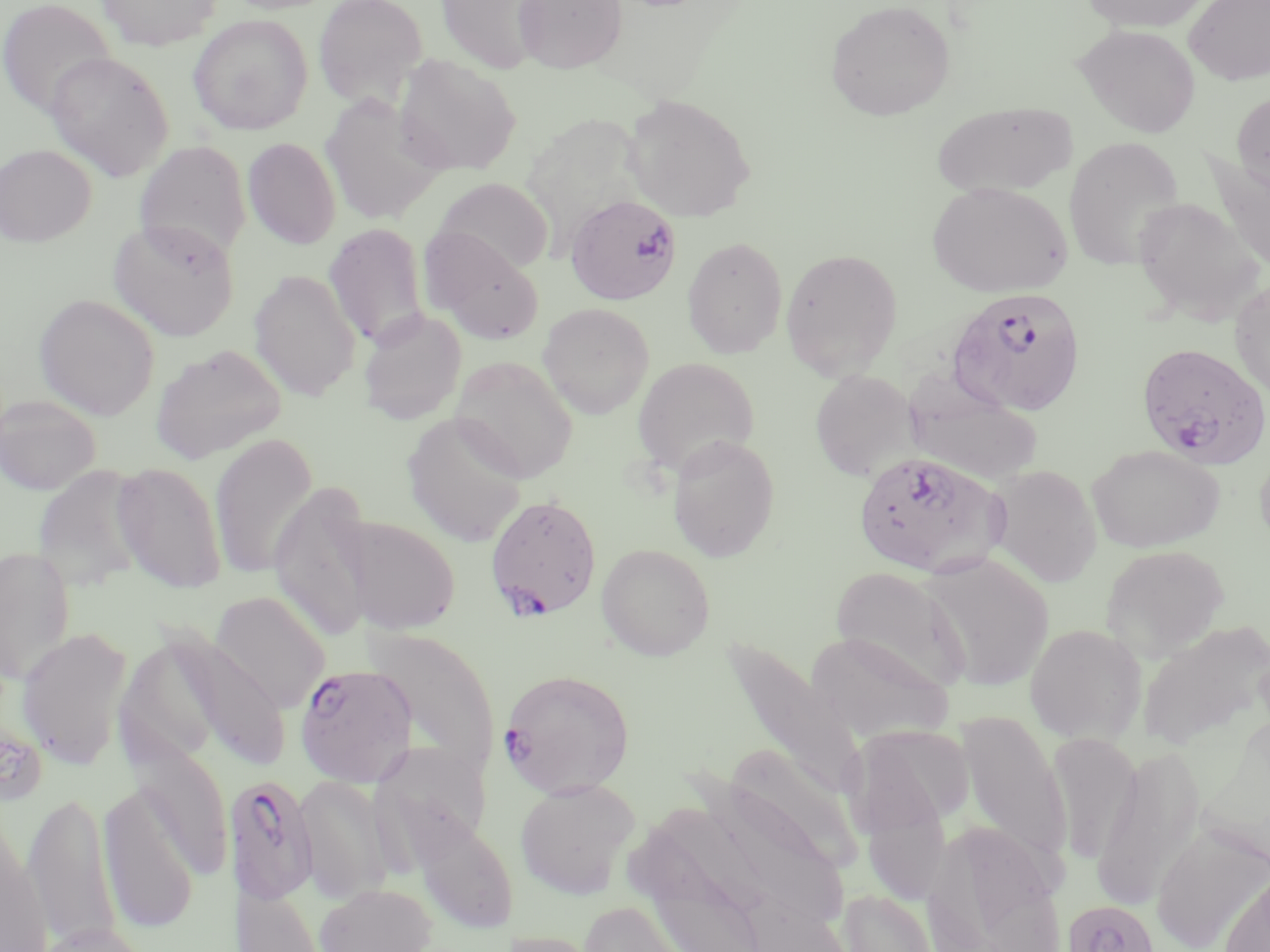

Approximate bounding boxes as [x1, y1, x2, y2] in pixels. Uninfected red blood cell locations: [96, 0, 221, 51], [313, 0, 428, 110], [435, 0, 549, 74], [513, 0, 627, 74], [825, 0, 956, 121], [1080, 0, 1211, 32], [1185, 0, 1270, 85], [0, 1, 115, 118], [188, 14, 312, 135], [1075, 24, 1200, 138], [45, 51, 174, 182], [392, 53, 521, 177], [1232, 91, 1270, 195], [621, 93, 755, 222], [319, 94, 444, 223], [931, 101, 1076, 198], [521, 114, 656, 235], [1063, 135, 1185, 271], [243, 137, 341, 249], [134, 140, 251, 263], [0, 143, 96, 247], [1204, 149, 1270, 277], [434, 177, 553, 275], [927, 181, 1072, 298], [1132, 197, 1263, 326], [108, 217, 240, 341], [324, 223, 430, 350], [422, 228, 545, 344], [682, 236, 788, 359], [780, 247, 903, 380], [249, 269, 361, 402], [1230, 277, 1270, 402], [33, 293, 161, 420], [538, 303, 654, 419], [358, 309, 467, 425], [150, 343, 287, 464], [449, 356, 578, 483], [633, 357, 759, 477], [810, 369, 921, 481], [902, 372, 1043, 486], [0, 393, 102, 496], [402, 412, 528, 547], [209, 433, 317, 580], [667, 433, 781, 562], [1253, 442, 1270, 559], [1087, 444, 1224, 553], [111, 461, 228, 594], [31, 465, 148, 590], [987, 465, 1103, 587], [269, 480, 375, 643], [341, 516, 461, 634], [596, 543, 715, 660], [0, 544, 77, 686], [1101, 544, 1230, 662], [920, 552, 1053, 691], [829, 565, 970, 692], [211, 591, 330, 712], [1136, 618, 1270, 753], [1024, 623, 1147, 744], [16, 627, 134, 770], [363, 627, 501, 777], [806, 630, 954, 743], [162, 631, 291, 772], [721, 637, 866, 800], [956, 711, 1071, 870], [847, 725, 974, 836], [1046, 732, 1141, 863], [375, 741, 490, 854], [720, 741, 863, 874], [130, 742, 234, 879], [1091, 746, 1207, 912], [294, 775, 394, 903], [515, 778, 640, 899], [99, 785, 200, 935], [24, 791, 122, 951], [0, 808, 51, 952], [409, 813, 518, 935], [921, 820, 1066, 952], [1151, 824, 1269, 951], [1219, 865, 1269, 952], [234, 880, 328, 951], [315, 883, 437, 952], [837, 888, 940, 952], [579, 900, 703, 952], [28, 922, 150, 952], [501, 929, 605, 952]. Plasmodium falciparum-infected red blood cell locations: [565, 195, 682, 305], [947, 288, 1087, 415], [1136, 341, 1270, 470], [852, 450, 1005, 579], [490, 499, 606, 624], [294, 662, 417, 788], [498, 668, 635, 797], [222, 774, 319, 906], [1062, 898, 1162, 952]. Slide-level diagnosis: Plasmodium falciparum. May-Grünwald-Giemsa stain. Image is 1270×952 pixels. Captured at 1000x magnification. Thin blood smear. Light microscopy. One field of a larger specimen.